Name the parasite shown.
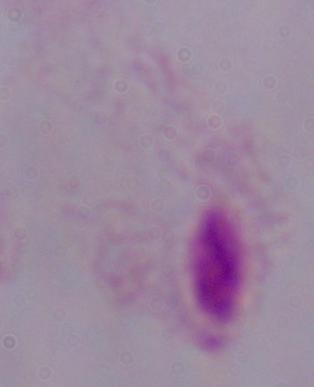

This is a trichomonad.

modality = micrograph
magnification = 1000x